State which parasite is depicted.
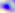

This is Toxoplasma gondii.

Summary:
  - Modality: photomicrograph
  - Magnification: 400x